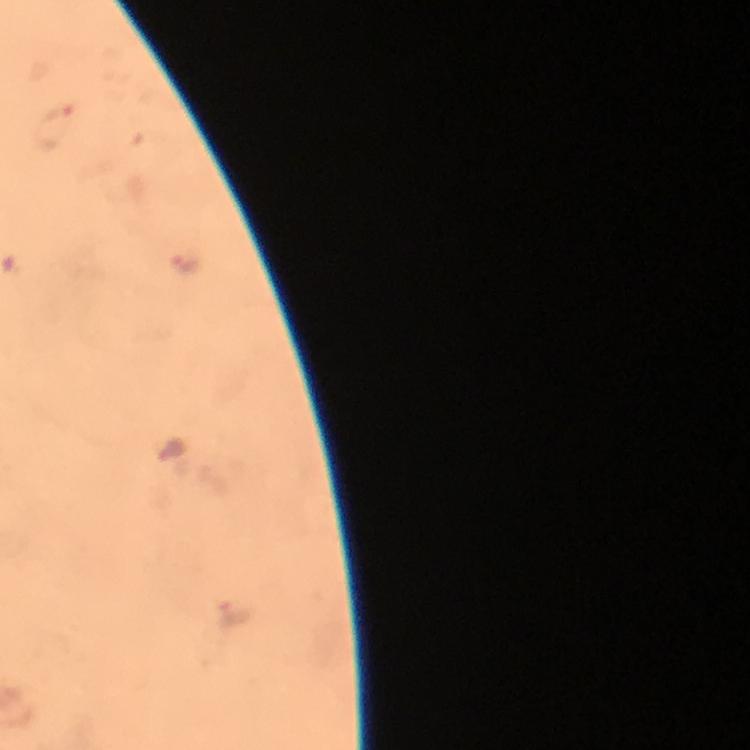

Approximate object centers, in pixels from the top-left corner. Malaria parasite locations: (x=55, y=126), (x=184, y=263), (x=169, y=445), (x=234, y=614). Immersion oil applied. Image is 750×750 pixels. 100x magnification. From a malaria diagnostic workup. Giemsa stain. Cropped region of a single field of view. Smartphone photograph taken through a microscope. Thick blood smear.